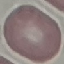
Result: negative for malaria parasites. Automatically extracted cell patch, resized to 64 × 64 pixels. Thin smear of blood. Giemsa-stained preparation. Acquired by smartphone through the microscope eyepiece.